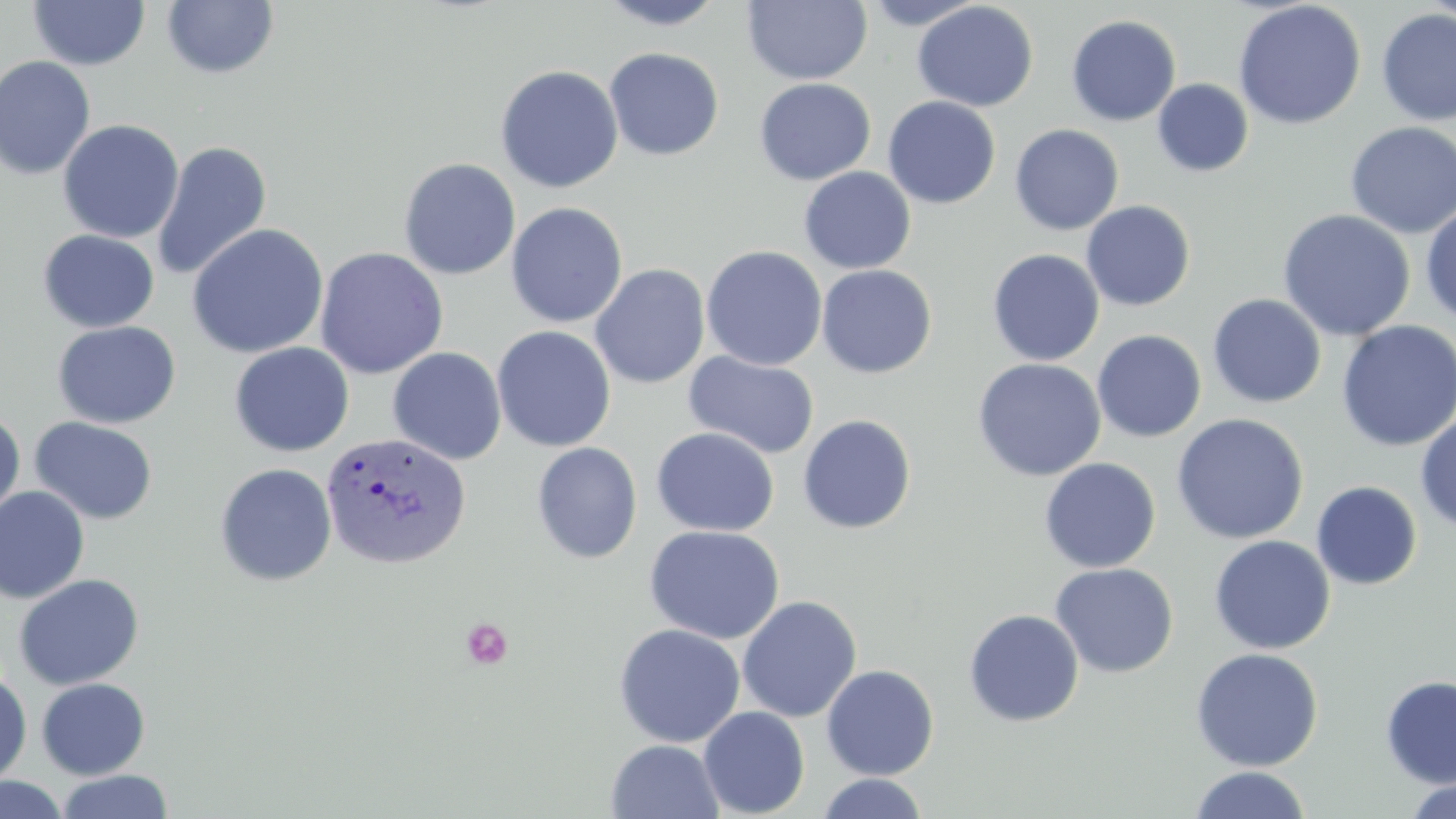
slide_level_diagnosis: Plasmodium vivax
modality: optical microscopy
field_of_view: one of a larger specimen
preparation: thin blood film
stain: May-Grünwald-Giemsa
platelet_locations: 'approximate bounding boxes as named x1/y1/x2/y2 corners in pixels: (x1=461, y1=617, x2=513, y2=669)'
magnification: 1000x
uninfected_red_blood_cell_locations: 'approximate bounding boxes as named x1/y1/x2/y2 corners in pixels: (x1=594, y1=0, x2=729, y2=30), (x1=858, y1=0, x2=986, y2=30), (x1=1420, y1=0, x2=1455, y2=24), (x1=28, y1=1, x2=150, y2=71), (x1=161, y1=1, x2=280, y2=80), (x1=741, y1=1, x2=873, y2=86), (x1=1232, y1=1, x2=1366, y2=130), (x1=912, y1=2, x2=1039, y2=112), (x1=1376, y1=8, x2=1455, y2=127), (x1=1066, y1=15, x2=1181, y2=126), (x1=603, y1=47, x2=724, y2=161), (x1=0, y1=55, x2=96, y2=180), (x1=495, y1=64, x2=623, y2=194), (x1=754, y1=78, x2=876, y2=185), (x1=1152, y1=78, x2=1254, y2=177), (x1=882, y1=96, x2=1001, y2=209), (x1=57, y1=119, x2=184, y2=244), (x1=1344, y1=122, x2=1456, y2=239), (x1=1009, y1=124, x2=1124, y2=235), (x1=152, y1=140, x2=272, y2=281), (x1=398, y1=158, x2=520, y2=280), (x1=799, y1=166, x2=916, y2=274), (x1=1081, y1=200, x2=1195, y2=312), (x1=505, y1=202, x2=628, y2=328), (x1=1420, y1=202, x2=1456, y2=325), (x1=1277, y1=208, x2=1416, y2=341), (x1=187, y1=223, x2=328, y2=359), (x1=37, y1=229, x2=159, y2=333), (x1=701, y1=245, x2=827, y2=371), (x1=314, y1=247, x2=449, y2=379), (x1=986, y1=248, x2=1104, y2=366), (x1=590, y1=264, x2=710, y2=389), (x1=817, y1=264, x2=937, y2=378), (x1=1207, y1=294, x2=1327, y2=408), (x1=52, y1=320, x2=181, y2=429), (x1=1336, y1=320, x2=1456, y2=452), (x1=492, y1=326, x2=616, y2=452), (x1=1092, y1=330, x2=1207, y2=443), (x1=229, y1=342, x2=354, y2=457), (x1=387, y1=347, x2=507, y2=466), (x1=684, y1=352, x2=820, y2=459), (x1=972, y1=357, x2=1107, y2=481), (x1=0, y1=407, x2=25, y2=526), (x1=1415, y1=412, x2=1456, y2=534), (x1=1171, y1=413, x2=1309, y2=544), (x1=797, y1=414, x2=917, y2=534), (x1=30, y1=416, x2=158, y2=525), (x1=651, y1=427, x2=779, y2=537), (x1=531, y1=442, x2=642, y2=564), (x1=1039, y1=457, x2=1161, y2=573), (x1=214, y1=463, x2=338, y2=587), (x1=1311, y1=480, x2=1422, y2=590), (x1=0, y1=486, x2=90, y2=604), (x1=645, y1=525, x2=784, y2=644), (x1=1209, y1=535, x2=1335, y2=654), (x1=1050, y1=563, x2=1178, y2=678), (x1=13, y1=573, x2=144, y2=690), (x1=737, y1=595, x2=862, y2=723), (x1=963, y1=609, x2=1085, y2=727), (x1=613, y1=623, x2=745, y2=747), (x1=1190, y1=647, x2=1324, y2=772), (x1=821, y1=664, x2=939, y2=780), (x1=0, y1=667, x2=33, y2=787), (x1=1380, y1=675, x2=1456, y2=789), (x1=36, y1=678, x2=150, y2=780), (x1=698, y1=706, x2=810, y2=818), (x1=605, y1=739, x2=725, y2=819), (x1=1189, y1=766, x2=1312, y2=819), (x1=56, y1=770, x2=173, y2=818), (x1=816, y1=773, x2=929, y2=819), (x1=0, y1=774, x2=70, y2=818), (x1=1400, y1=779, x2=1455, y2=819)'
image_size: 1456×819 pixels
plasmodium_vivax_infected_red_blood_cell_locations: 'approximate bounding boxes as named x1/y1/x2/y2 corners in pixels: (x1=319, y1=432, x2=472, y2=571)'